State which parasite is depicted.
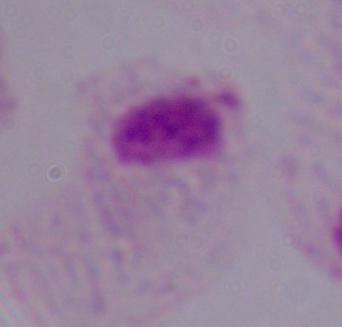
A trichomonad.

Summary:
  - Modality: photomicrograph
  - Magnification: 1000x